Comment on the morphology of the red blood cells.
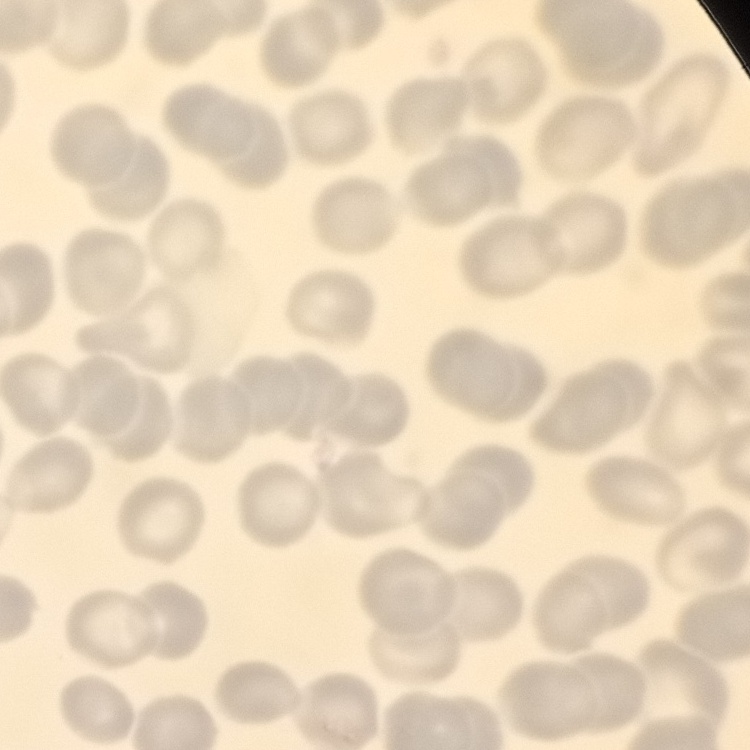

No rouleaux formation.

{
  "preparation": "thin blood smear",
  "image_type": "one tile cut from a larger photomicrograph",
  "stain": "Field's or Giemsa"
}